Comment on the morphology of the red blood cells.
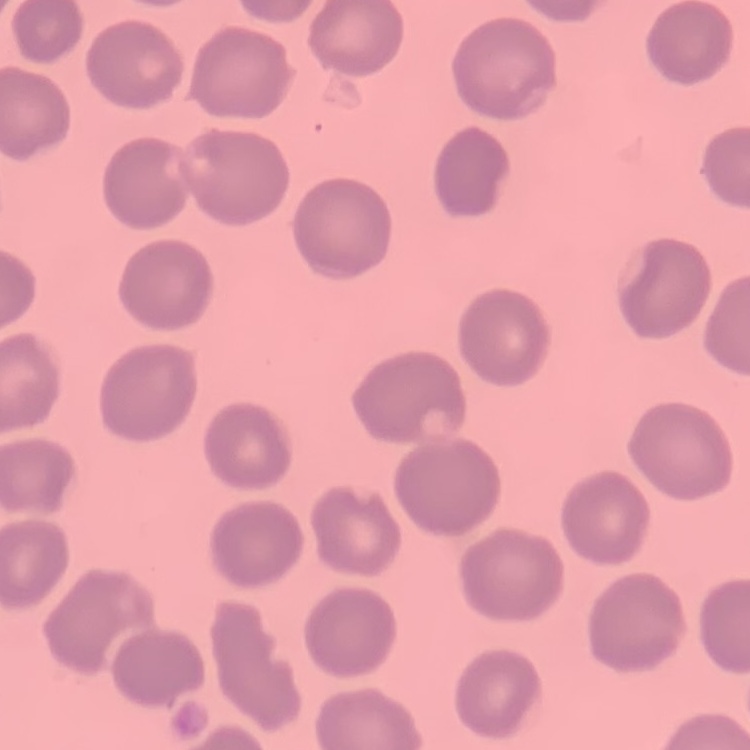
They show no rouleaux formation.

Summary:
  - Stain: Field's or Giemsa
  - Image type: one tile cut from a larger photomicrograph
  - Preparation: thin peripheral smear